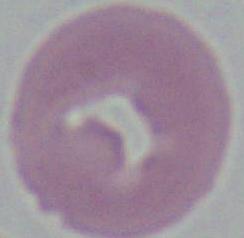

{
  "magnification": "1000x",
  "identification": "red blood cell",
  "modality": "photomicrograph"
}